Name the parasite shown.
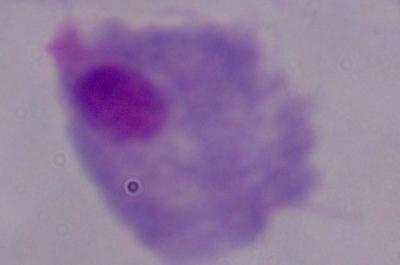
This is a trichomonad.

modality: micrograph
magnification: 1000x